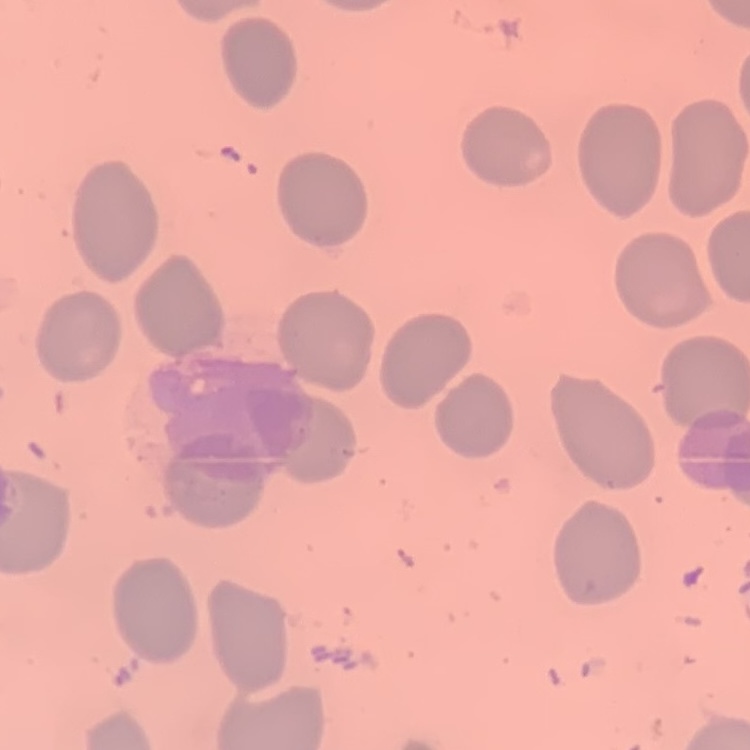
Summary:
  - Red blood cell morphology: no rouleaux formation
  - Image type: square crop of a larger photomicrograph
  - Stain: Field's or Giemsa
  - Preparation: thin blood film